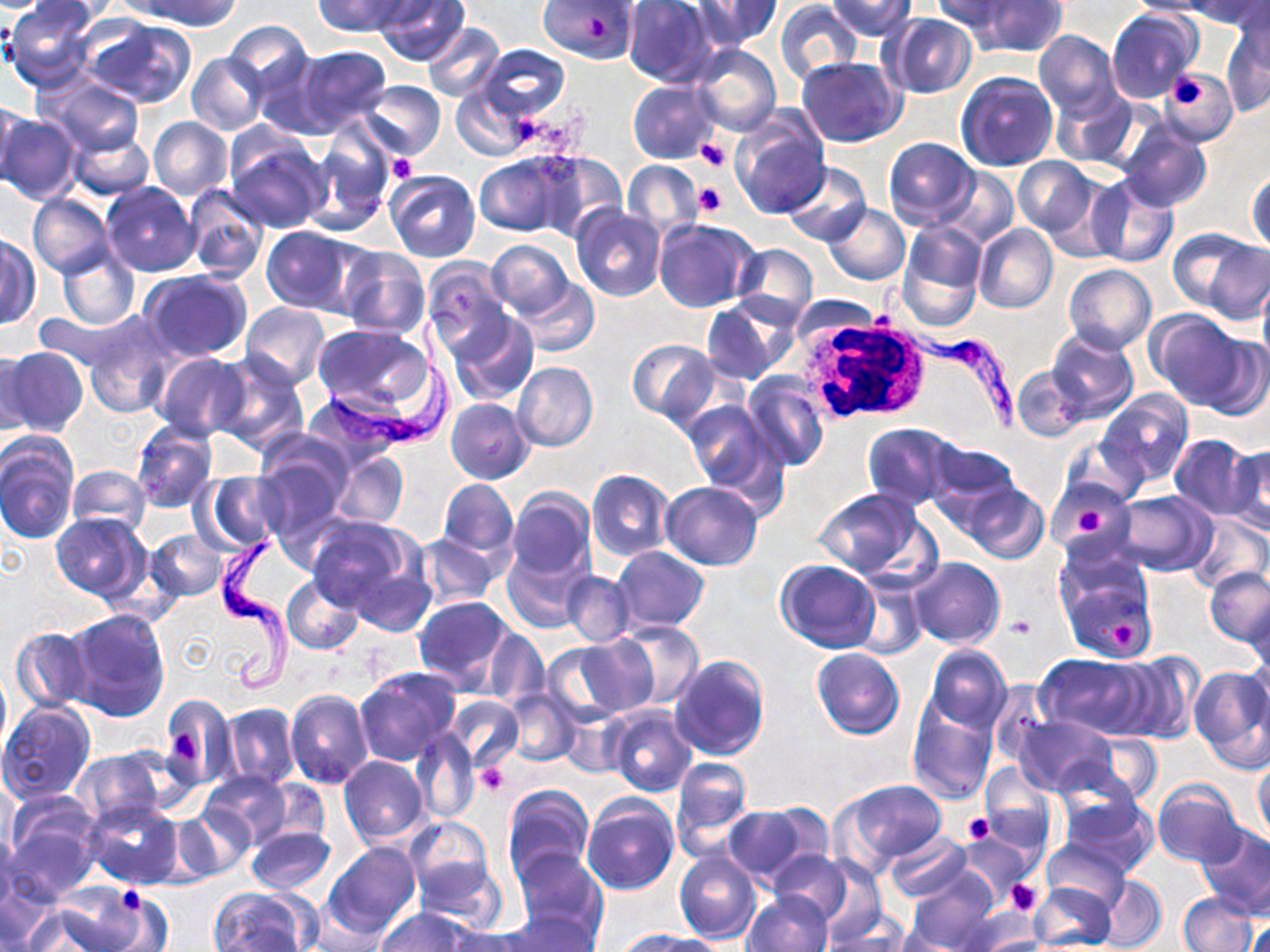
slide-level diagnosis = Trypanosoma brucei
white blood cell locations = approximate bounding boxes as (x1, y1, x2, y2) in pixels: (788, 311, 932, 425)
magnification = 1000x
uninfected red blood cell locations = approximate bounding boxes as (x1, y1, x2, y2) in pixels: (4, 0, 99, 91), (135, 0, 245, 30), (313, 0, 409, 37), (373, 0, 470, 66), (537, 0, 639, 64), (693, 0, 781, 48), (827, 0, 916, 41), (931, 0, 1020, 38), (1123, 0, 1213, 17), (1186, 0, 1269, 28), (622, 1, 718, 87), (975, 1, 1066, 57), (774, 2, 862, 83), (1106, 8, 1200, 103), (885, 14, 976, 98), (84, 18, 196, 108), (224, 22, 313, 99), (423, 24, 505, 102), (1222, 25, 1268, 114), (1034, 30, 1121, 119), (475, 44, 569, 122), (290, 45, 392, 135), (691, 45, 781, 135), (187, 51, 268, 135), (797, 56, 906, 147), (1160, 69, 1236, 142), (957, 71, 1057, 171), (36, 73, 146, 157), (357, 80, 445, 160), (629, 80, 718, 164), (450, 85, 532, 160), (1052, 87, 1141, 169), (0, 96, 22, 192), (1, 112, 81, 205), (731, 112, 831, 220), (148, 115, 234, 199), (1118, 121, 1211, 213), (309, 126, 393, 228), (69, 131, 153, 200), (226, 136, 329, 234), (883, 136, 978, 225), (530, 152, 628, 242), (474, 153, 569, 236), (1014, 156, 1097, 239), (623, 160, 704, 237), (781, 162, 872, 247), (937, 168, 1020, 247), (385, 171, 481, 263), (1248, 171, 1269, 256), (1085, 174, 1180, 270), (102, 182, 200, 277), (184, 184, 270, 283), (27, 194, 113, 277), (824, 204, 910, 285), (571, 206, 665, 301), (654, 219, 757, 312), (896, 223, 986, 330), (973, 224, 1058, 313), (260, 227, 361, 315), (0, 233, 39, 329), (1196, 235, 1270, 325), (486, 239, 576, 318), (731, 244, 818, 326), (55, 246, 139, 330), (338, 247, 429, 340), (420, 257, 511, 355), (1063, 264, 1155, 353), (140, 269, 253, 360), (1258, 276, 1270, 375), (514, 277, 599, 355), (701, 297, 792, 385), (239, 302, 331, 388), (34, 307, 138, 373), (1147, 310, 1245, 407), (447, 311, 538, 406), (84, 314, 175, 418), (312, 323, 434, 414), (1046, 331, 1137, 424), (1197, 332, 1270, 421), (626, 339, 718, 425), (2, 346, 89, 438), (0, 349, 42, 435), (151, 351, 251, 440), (210, 354, 307, 454), (513, 362, 598, 452), (1013, 367, 1087, 441), (743, 374, 830, 473), (1098, 390, 1193, 486), (302, 392, 413, 472), (446, 397, 535, 485), (680, 401, 783, 501), (131, 420, 218, 513), (862, 422, 956, 510), (1064, 433, 1147, 505), (0, 435, 79, 544), (1169, 435, 1258, 519), (253, 441, 350, 534), (929, 442, 1021, 518), (1226, 445, 1270, 533), (330, 449, 409, 529), (66, 465, 151, 541), (586, 469, 674, 562), (201, 471, 285, 550), (1047, 478, 1135, 555), (438, 479, 517, 558), (660, 481, 763, 571), (963, 484, 1048, 563), (506, 488, 595, 582), (812, 489, 932, 580), (1110, 491, 1217, 577), (53, 513, 151, 602), (1186, 513, 1268, 593), (307, 517, 420, 620), (146, 528, 227, 601), (415, 533, 500, 608), (503, 544, 592, 632), (614, 546, 709, 632), (1052, 549, 1158, 665), (339, 555, 436, 638), (910, 557, 1005, 649), (775, 558, 880, 653), (1206, 566, 1270, 646), (561, 571, 634, 645), (850, 574, 928, 659), (281, 575, 363, 655), (414, 596, 513, 691), (1247, 600, 1270, 689), (64, 608, 170, 722), (613, 620, 705, 708), (11, 627, 91, 713), (480, 628, 549, 708), (563, 634, 659, 719), (1246, 643, 1270, 730), (924, 645, 1011, 734), (812, 648, 905, 739), (1114, 651, 1203, 744), (668, 653, 770, 760), (1034, 654, 1154, 738), (1189, 666, 1270, 769), (0, 667, 10, 754), (353, 667, 463, 768), (985, 683, 1056, 770), (285, 688, 373, 787), (503, 689, 582, 765), (159, 693, 236, 792), (446, 695, 525, 771), (0, 701, 96, 803), (907, 702, 999, 804), (222, 704, 300, 789), (605, 706, 697, 796), (558, 708, 632, 778), (1011, 714, 1116, 797), (410, 729, 480, 823), (1074, 733, 1162, 807), (72, 750, 167, 832), (339, 755, 429, 846), (671, 756, 754, 858), (1254, 759, 1270, 840), (980, 764, 1055, 852), (202, 771, 293, 848), (1151, 778, 1245, 867), (255, 780, 330, 848), (842, 781, 946, 866), (503, 784, 593, 885), (1059, 794, 1159, 876), (582, 796, 679, 896), (84, 798, 184, 889), (5, 800, 103, 898), (758, 804, 836, 871), (722, 805, 809, 884), (178, 806, 256, 881), (404, 816, 495, 913), (1196, 823, 1270, 917), (0, 827, 18, 917), (247, 827, 335, 894), (882, 830, 972, 903), (955, 832, 1035, 907), (1041, 837, 1130, 911), (324, 844, 420, 939), (673, 850, 762, 943), (514, 851, 607, 949), (767, 851, 851, 926), (790, 856, 883, 938), (904, 871, 997, 950), (2, 873, 52, 950), (1096, 876, 1167, 950), (1028, 881, 1117, 952), (46, 884, 161, 952), (207, 888, 314, 952), (741, 892, 834, 952), (1178, 893, 1257, 952), (306, 901, 389, 951), (950, 907, 1041, 951), (375, 908, 473, 952), (502, 908, 601, 952), (826, 909, 911, 951), (1244, 910, 1268, 952), (443, 928, 533, 952), (626, 932, 726, 952)
modality = light microscopy
field of view = one of a larger specimen
platelet locations = approximate bounding boxes as (x1, y1, x2, y2) in pixels: (1164, 71, 1207, 112), (696, 138, 730, 171), (387, 154, 417, 182), (692, 183, 726, 218), (1075, 507, 1108, 545), (1006, 613, 1037, 639), (1108, 622, 1136, 650), (172, 729, 199, 769), (476, 762, 510, 796), (964, 812, 996, 844), (1008, 880, 1043, 916), (116, 887, 146, 915)
Trypanosoma brucei locations = approximate bounding boxes as (x1, y1, x2, y2) in pixels: (887, 289, 1027, 437), (326, 302, 468, 461), (212, 534, 308, 701)
preparation = thin blood smear
image size = 1270×952 pixels
stain = May-Grünwald-Giemsa